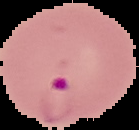

Summary:
  - Image type: segmented cell region on a black background
  - Malaria status: parasitized
  - Image size: 139×130 pixels
  - Preparation: thin blood smear